State the preparation type.
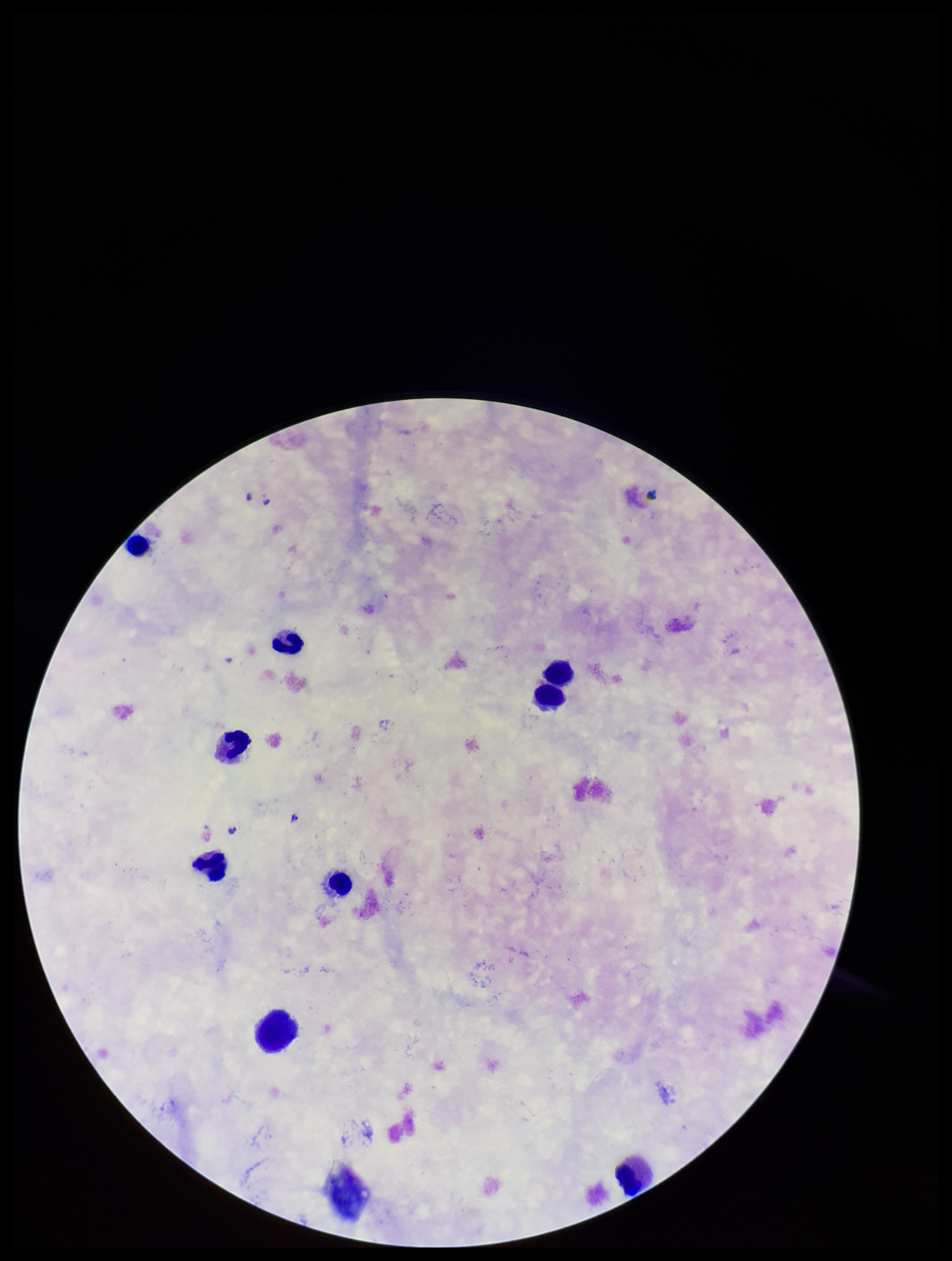

A thick smear.

One field from this slide. Stained with Giemsa. Parasite count: 2. Patient malaria status: infected. Species reported for this patient: Plasmodium falciparum. Photographed through the microscope eyepiece with a smartphone camera. Plasmodium parasites: seen. Leukocyte count: 8. Image is 952×1261 pixels.